Outline each Plasmodium ovale-infected red blood cell.
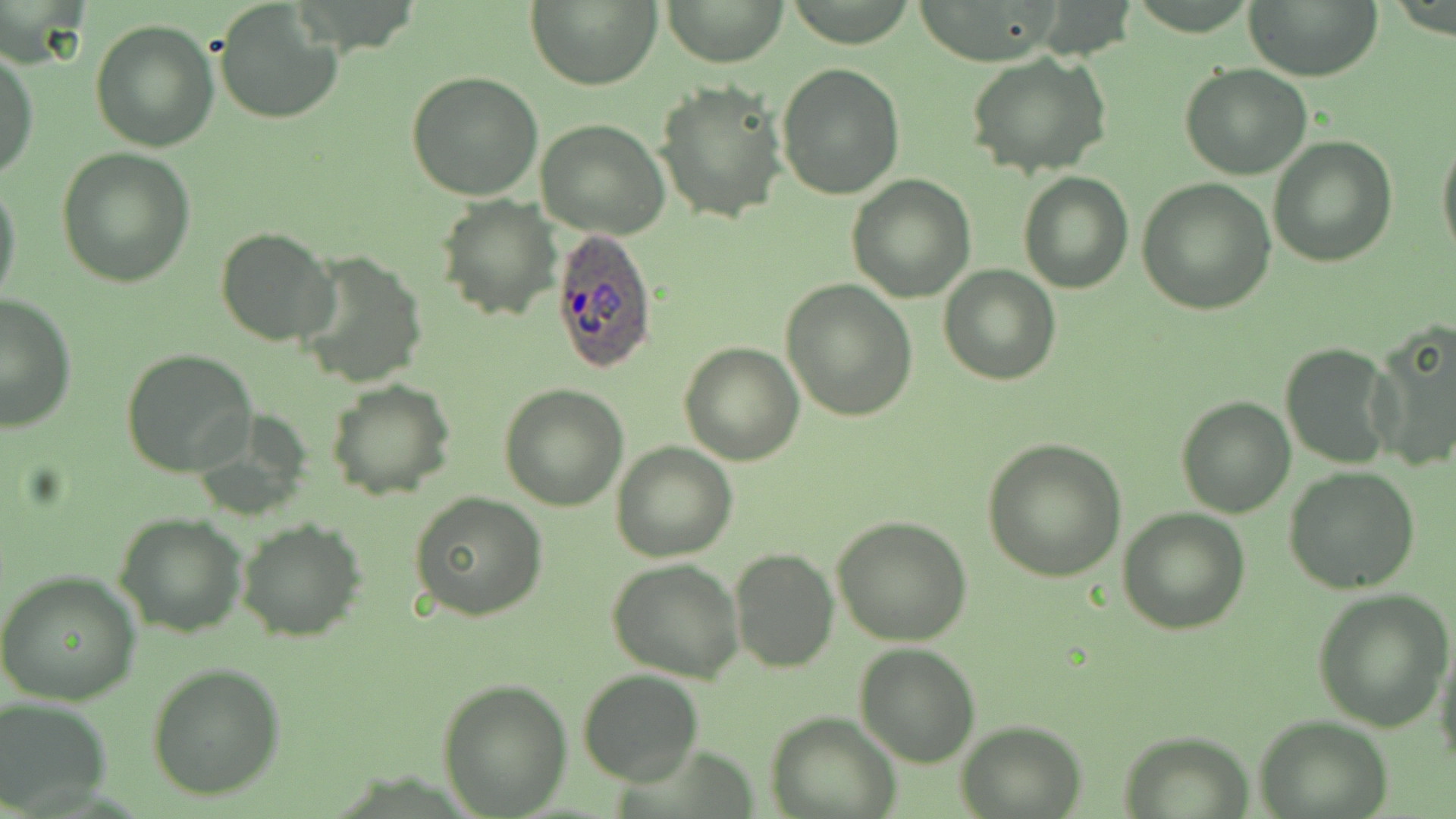

Approximate bounding boxes as named x1/y1/x2/y2 corners in pixels.
Plasmodium ovale-infected red blood cells: (x1=550, y1=229, x2=659, y2=373).

Uninfected red blood cell locations: (x1=527, y1=0, x2=661, y2=90), (x1=660, y1=0, x2=788, y2=65), (x1=1245, y1=0, x2=1383, y2=80), (x1=212, y1=2, x2=343, y2=126), (x1=89, y1=19, x2=220, y2=154), (x1=0, y1=44, x2=38, y2=180), (x1=966, y1=51, x2=1112, y2=179), (x1=777, y1=62, x2=905, y2=198), (x1=1180, y1=65, x2=1314, y2=180), (x1=405, y1=71, x2=544, y2=201), (x1=654, y1=81, x2=787, y2=225), (x1=537, y1=120, x2=670, y2=239), (x1=1437, y1=129, x2=1456, y2=266), (x1=1269, y1=136, x2=1397, y2=267), (x1=57, y1=147, x2=196, y2=287), (x1=1018, y1=171, x2=1135, y2=293), (x1=846, y1=175, x2=975, y2=302), (x1=0, y1=176, x2=22, y2=313), (x1=1136, y1=177, x2=1277, y2=316), (x1=436, y1=196, x2=560, y2=322), (x1=215, y1=227, x2=338, y2=347), (x1=294, y1=249, x2=430, y2=390), (x1=939, y1=265, x2=1062, y2=384), (x1=781, y1=278, x2=917, y2=421), (x1=0, y1=291, x2=76, y2=432), (x1=1367, y1=320, x2=1456, y2=475), (x1=680, y1=342, x2=804, y2=465), (x1=1280, y1=343, x2=1396, y2=470), (x1=121, y1=349, x2=258, y2=478), (x1=325, y1=380, x2=456, y2=500), (x1=498, y1=383, x2=629, y2=511), (x1=1175, y1=395, x2=1295, y2=518), (x1=984, y1=437, x2=1126, y2=581), (x1=611, y1=441, x2=737, y2=562), (x1=1285, y1=467, x2=1420, y2=594), (x1=408, y1=491, x2=549, y2=622), (x1=1118, y1=508, x2=1250, y2=635), (x1=114, y1=512, x2=248, y2=637), (x1=831, y1=516, x2=973, y2=646), (x1=237, y1=518, x2=365, y2=641), (x1=729, y1=548, x2=839, y2=673), (x1=609, y1=559, x2=745, y2=681), (x1=0, y1=569, x2=142, y2=706), (x1=1311, y1=588, x2=1453, y2=730), (x1=1433, y1=633, x2=1456, y2=768), (x1=853, y1=643, x2=982, y2=768), (x1=147, y1=664, x2=285, y2=800), (x1=578, y1=670, x2=705, y2=786), (x1=436, y1=677, x2=573, y2=817), (x1=0, y1=698, x2=111, y2=812), (x1=767, y1=711, x2=899, y2=818), (x1=1254, y1=715, x2=1394, y2=818), (x1=954, y1=720, x2=1087, y2=817), (x1=1119, y1=731, x2=1254, y2=817). Slide-level diagnosis: Plasmodium ovale. Thin blood smear. Image is 1456×819 pixels. One field of a larger specimen. May-Grünwald-Giemsa stain. Captured at 1000x magnification. Light microscopy.